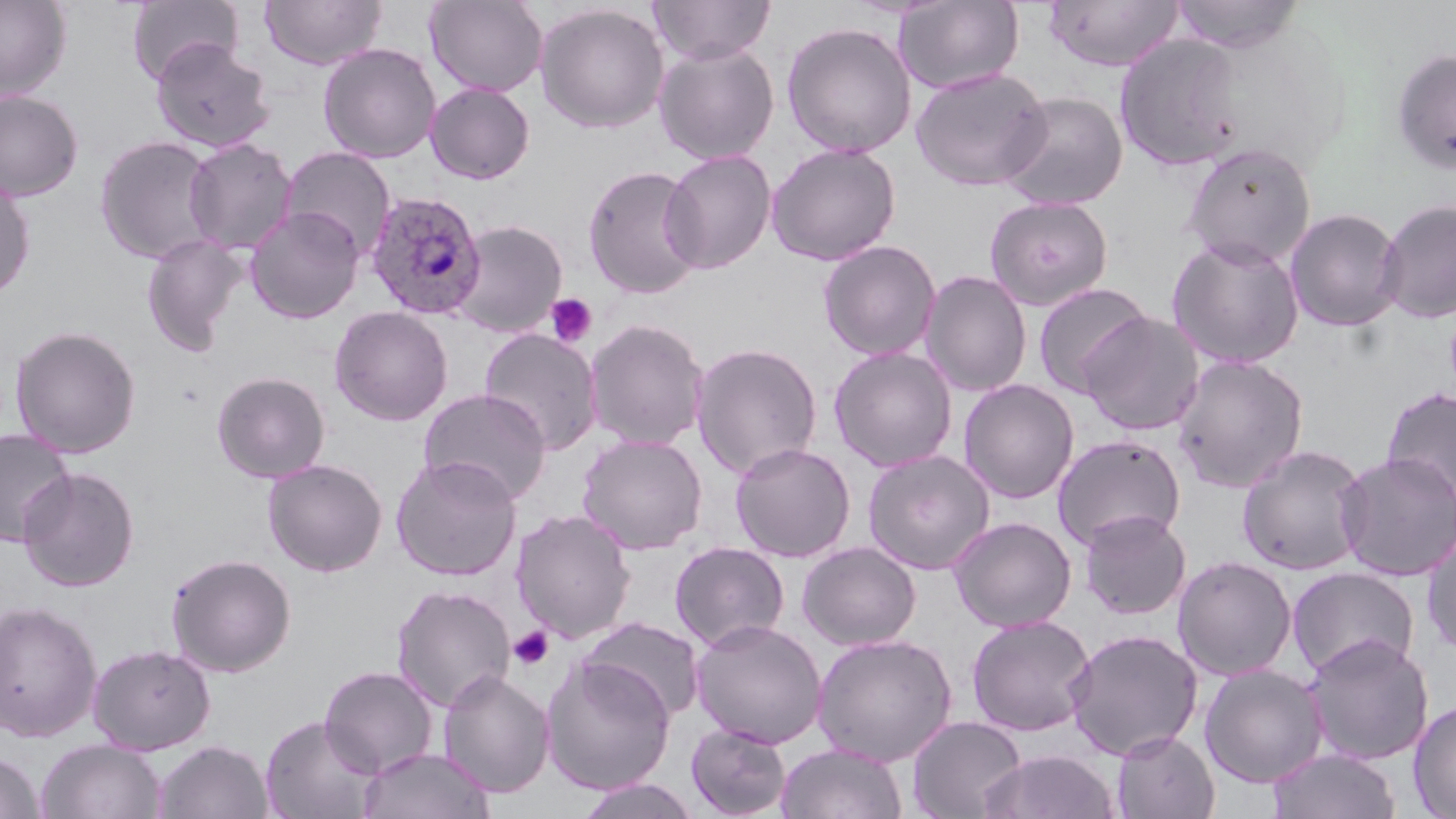
slide_level_diagnosis: Plasmodium ovale
platelet_locations: 'approximate bounding boxes as (x1,y1)-(x2,y2) corner pairs in pixels: (544,293)-(598,348), (508,625)-(555,671)'
preparation: thin blood smear
magnification: 1000x
uninfected_red_blood_cell_locations: 'approximate bounding boxes as (x1,y1)-(x2,y2) corner pairs in pixels: (0,0)-(72,101), (127,0)-(244,85), (259,0)-(387,71), (424,0)-(548,97), (648,0)-(776,65), (895,0)-(1024,94), (1042,0)-(1184,72), (1169,0)-(1304,53), (534,3)-(670,134), (781,22)-(917,158), (1114,33)-(1243,172), (151,40)-(275,154), (653,41)-(780,165), (318,42)-(441,163), (1389,48)-(1456,176), (910,66)-(1052,191), (424,81)-(536,184), (0,90)-(84,201), (998,91)-(1129,210), (95,135)-(220,265), (183,137)-(298,256), (766,142)-(901,266), (1182,143)-(1317,269), (279,146)-(397,260), (660,149)-(777,274), (582,164)-(704,300), (0,176)-(36,300), (985,196)-(1114,311), (1376,198)-(1456,325), (245,206)-(365,324), (1285,207)-(1404,332), (451,220)-(568,337), (141,233)-(247,356), (1166,237)-(1305,370), (818,240)-(941,361), (920,270)-(1032,397), (1033,282)-(1154,398), (329,305)-(453,426), (1078,311)-(1206,436), (584,318)-(710,451), (9,324)-(142,458), (478,328)-(603,455), (690,342)-(823,479), (828,345)-(958,472), (1171,354)-(1309,493), (211,371)-(331,483), (959,379)-(1080,504), (1381,386)-(1456,502), (417,388)-(553,506), (0,427)-(76,548), (576,433)-(708,554), (1052,435)-(1186,551), (730,442)-(856,563), (1237,444)-(1370,576), (862,448)-(995,575), (1334,452)-(1456,582), (390,455)-(522,581), (262,458)-(388,578), (17,466)-(140,593), (511,508)-(637,644), (1078,510)-(1192,620), (948,516)-(1077,632), (1421,526)-(1456,657), (801,533)-(941,740), (669,541)-(791,652), (796,541)-(922,651), (166,552)-(297,677), (1172,555)-(1297,681), (1287,566)-(1420,680), (391,584)-(516,713), (0,599)-(102,742), (966,615)-(1096,736), (579,616)-(705,721), (690,619)-(827,748), (1064,628)-(1204,761), (812,633)-(957,766), (1303,634)-(1434,765), (87,643)-(216,755), (540,655)-(676,795), (1199,663)-(1328,788), (318,665)-(439,778), (438,669)-(555,797), (1408,699)-(1456,818), (259,714)-(381,818), (907,716)-(1027,818), (686,723)-(792,819), (1112,730)-(1220,819), (36,739)-(166,819), (154,740)-(274,819), (776,742)-(907,819), (358,746)-(496,819), (1267,747)-(1401,819), (979,749)-(1121,819), (0,753)-(45,819), (574,778)-(701,819)'
image_size: 1456×819 pixels
plasmodium_ovale_infected_red_blood_cell_locations: 'approximate bounding boxes as (x1,y1)-(x2,y2) corner pairs in pixels: (365,191)-(487,321)'
field_of_view: single
stain: May-Grünwald-Giemsa
modality: optical microscopy